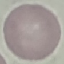

result = no malaria parasites seen
preparation = thin blood film
stain = Giemsa
capture = smartphone camera at the microscope eyepiece
image type = automatically extracted cell patch, resized to 64 × 64 pixels